Assess this cell for malaria.
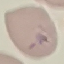

Parasitized.

{
  "preparation": "thin smear",
  "capture": "smartphone camera at the microscope eyepiece",
  "image_type": "automatically extracted cell patch, resized to 64 × 64 pixels",
  "stain": "Giemsa"
}